Assess the morphology of the red blood cells.
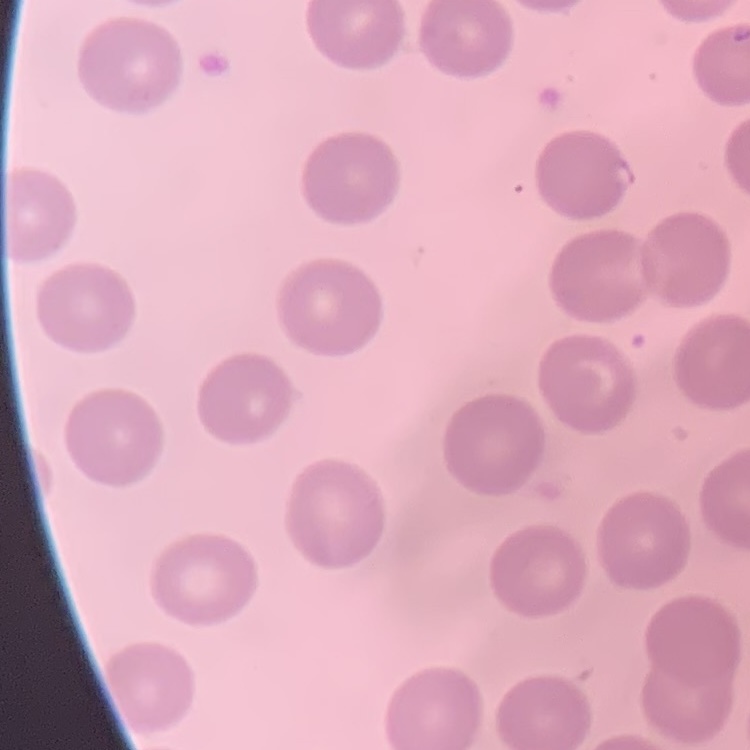

No rouleaux formation.

Square crop of a larger photomicrograph. Thin blood film. Field's or Giemsa stain.